Identify the cell.
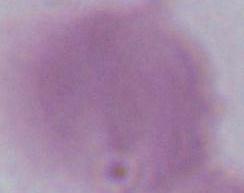

This is an erythrocyte.

magnification = 1000x
modality = photomicrograph